Report the malaria status of this cell.
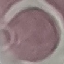
It is uninfected.

Summary:
  - Image type: automatically extracted cell patch, resized to 64 × 64 pixels
  - Stain: Giemsa
  - Capture: smartphone through the microscope eyepiece
  - Preparation: thin blood smear